Assess the morphology of the erythrocytes.
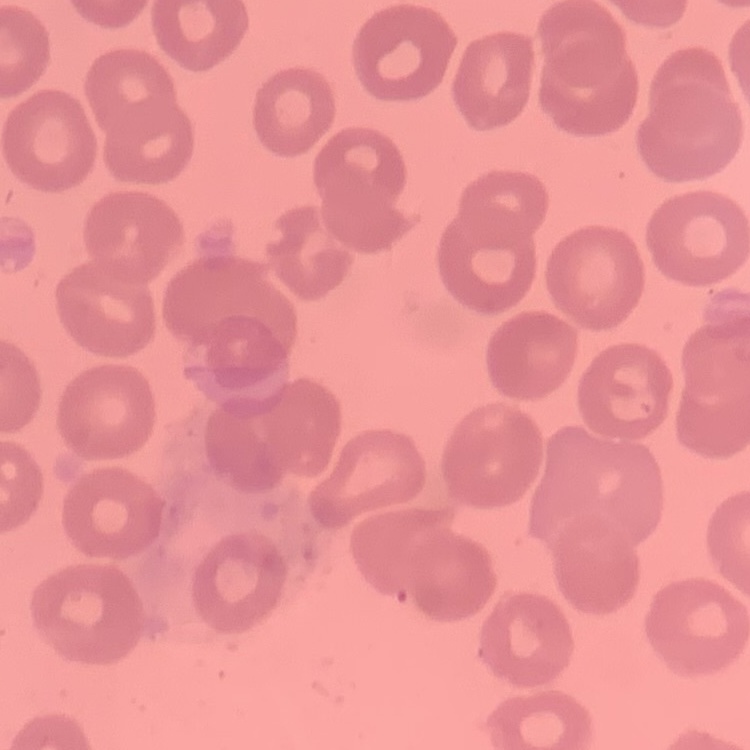
No rouleaux formation.

Field's or Giemsa stain. Square crop of a larger photomicrograph. Thin blood smear.